Outline platelets.
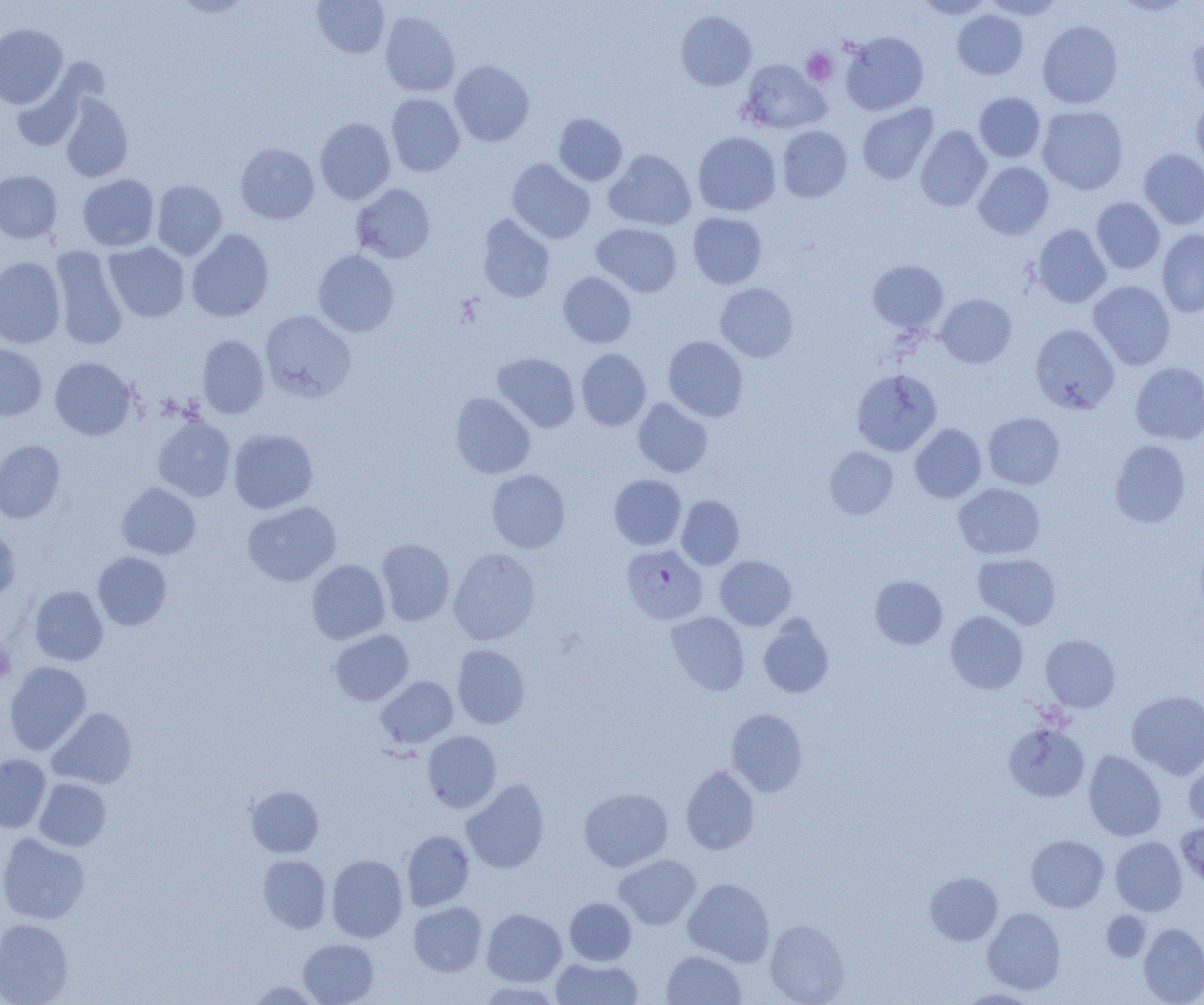
Approximate bounding boxes as (x1,y1)-(x2,y2) corner pairs in pixels.
Platelets: (801,48)-(837,85), (0,643)-(15,682).

slide_level_diagnosis: Plasmodium falciparum
uninfected_red_blood_cell_locations: 'approximate bounding boxes as (x1,y1)-(x2,y2) corner pairs in pixels: (312,0)-(389,58), (915,0)-(993,19), (981,0)-(1064,20), (676,10)-(756,91), (952,10)-(1028,79), (380,11)-(460,97), (1037,20)-(1123,109), (0,23)-(68,108), (841,31)-(928,116), (1187,33)-(1204,106), (739,59)-(831,135), (450,60)-(534,147), (11,74)-(88,151), (974,92)-(1046,163), (59,93)-(133,182), (386,94)-(465,176), (1191,97)-(1204,173), (857,103)-(938,184), (1037,105)-(1128,194), (553,113)-(627,186), (314,118)-(396,204), (916,125)-(992,211), (777,126)-(853,202), (692,131)-(781,216), (235,143)-(319,224), (605,149)-(695,230), (1139,149)-(1204,229), (507,159)-(595,244), (973,162)-(1054,239), (0,170)-(62,243), (77,174)-(159,251), (151,180)-(227,260), (352,184)-(435,264), (1092,197)-(1165,274), (687,212)-(767,289), (477,213)-(556,302), (592,223)-(681,297), (1032,224)-(1111,308), (186,229)-(274,322), (1157,229)-(1204,317), (104,242)-(189,322), (50,245)-(128,351), (313,249)-(399,336), (0,256)-(65,348), (868,260)-(948,332), (558,272)-(636,348), (1088,281)-(1176,370), (715,282)-(798,362), (936,294)-(1017,368), (260,310)-(355,401), (1030,324)-(1119,414), (197,335)-(269,419), (663,336)-(748,421), (0,343)-(47,420), (576,348)-(651,430), (492,352)-(580,432), (50,358)-(137,440), (1131,362)-(1204,444), (851,368)-(942,456), (450,392)-(535,479), (633,398)-(713,477), (983,412)-(1065,489), (153,417)-(235,501), (910,423)-(987,503), (229,428)-(318,514), (1110,439)-(1191,527), (0,440)-(65,523), (825,446)-(899,520), (486,469)-(570,553), (609,474)-(686,550), (117,482)-(201,559), (953,482)-(1046,560), (676,495)-(744,569), (242,501)-(341,586), (0,527)-(20,603), (376,538)-(455,625), (448,548)-(540,645), (93,552)-(172,630), (973,552)-(1061,629), (715,555)-(796,630), (307,559)-(390,645), (869,575)-(947,649), (29,585)-(108,665), (667,611)-(749,695), (946,611)-(1028,694), (758,615)-(834,698), (330,629)-(413,705), (1041,634)-(1120,711), (452,644)-(530,728), (4,662)-(91,755), (376,676)-(458,748), (1127,690)-(1204,779), (47,707)-(137,789), (726,709)-(808,796), (1004,722)-(1090,802), (422,731)-(501,812), (1083,750)-(1166,841), (0,754)-(51,833), (1184,756)-(1204,828), (681,766)-(759,854), (34,778)-(111,851), (461,779)-(549,873), (246,786)-(324,857), (579,787)-(673,871), (1176,822)-(1204,889), (401,830)-(474,911), (0,833)-(90,925), (1026,835)-(1109,912), (1110,836)-(1187,915), (258,854)-(331,933), (326,854)-(408,942), (613,854)-(701,929), (925,872)-(1003,945), (683,878)-(774,967), (564,897)-(636,965), (408,902)-(486,976), (983,907)-(1066,994), (481,908)-(567,986), (1102,911)-(1150,962), (0,918)-(74,1004), (765,919)-(850,1004), (1138,923)-(1204,1005), (298,938)-(378,1005), (662,950)-(746,1005), (550,957)-(643,1004), (246,980)-(322,1004), (476,981)-(564,1004), (957,988)-(1041,1004)'
modality: optical microscopy
field_of_view: one of a larger specimen
preparation: thin blood smear
magnification: 1000x
plasmodium_falciparum_infected_red_blood_cell_locations: 'approximate bounding boxes as (x1,y1)-(x2,y2) corner pairs in pixels: (622,544)-(707,625)'
image_size: 1204×1005 pixels